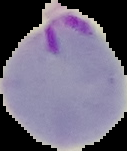
Result: malaria parasites identified. Image is 127×151 pixels. The area outside the segmented cell region is set to black. From a thin blood smear.